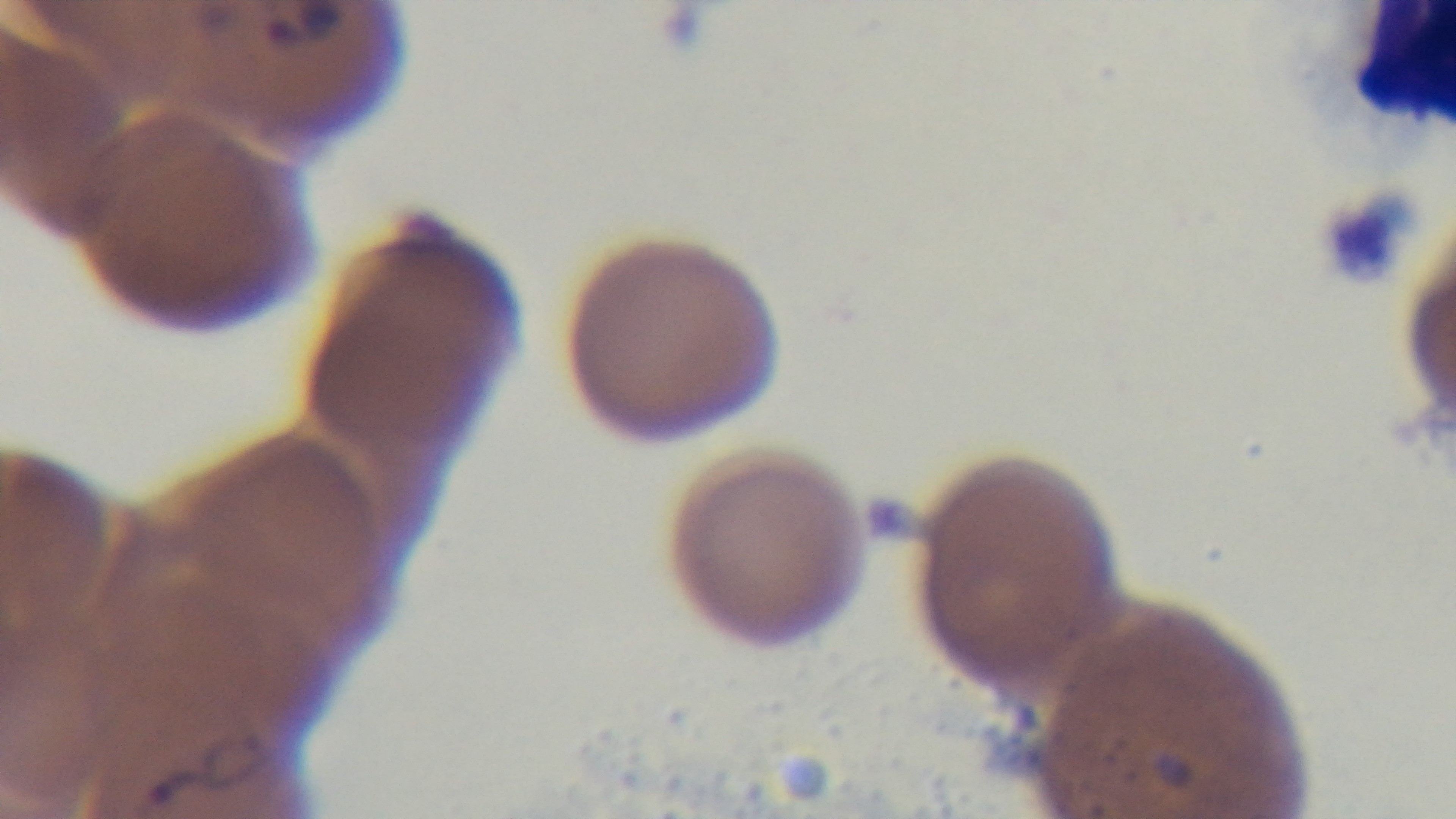
Captured with a mounted 4K digital camera. Giemsa-stained. One field from the slide. Preparation: thin. 100x oil-immersion objective. Photomicrograph. Malaria status: infected.